State the blood parasite species.
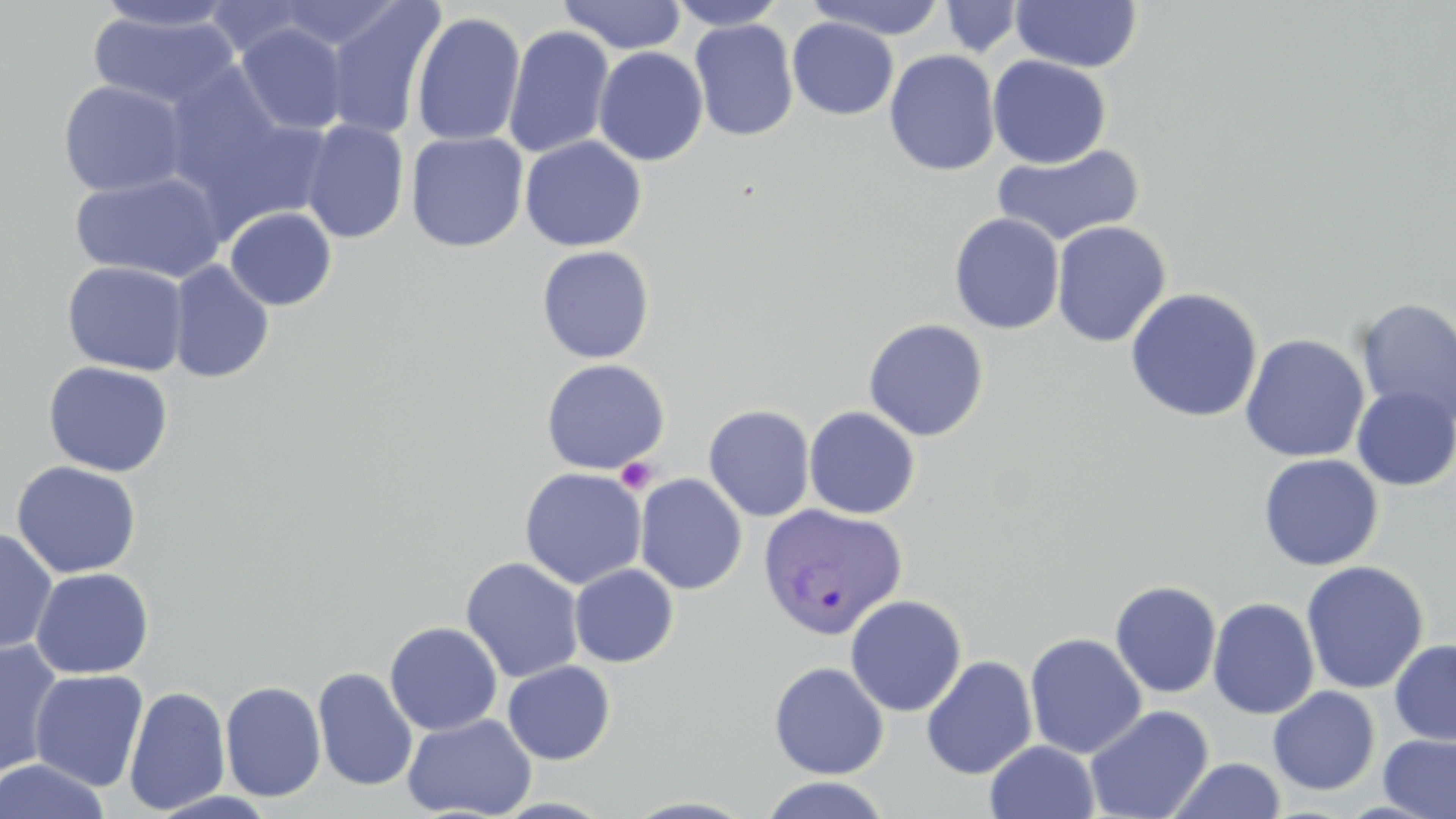
Plasmodium vivax.

Approximate bounding boxes as [x1, y1, x2, y2] in pixels. Plasmodium vivax-infected red blood cell locations: [758, 502, 907, 639]. Uninfected red blood cell locations: [89, 0, 241, 33], [321, 0, 444, 141], [558, 0, 687, 54], [666, 0, 788, 30], [804, 0, 950, 40], [202, 1, 324, 60], [939, 1, 1025, 58], [1009, 1, 1144, 72], [87, 8, 242, 112], [410, 11, 526, 147], [786, 17, 898, 120], [689, 19, 799, 142], [234, 23, 351, 136], [503, 24, 614, 158], [593, 46, 709, 166], [884, 49, 1001, 177], [987, 55, 1112, 169], [158, 65, 306, 215], [56, 79, 190, 197], [192, 109, 339, 238], [300, 120, 409, 243], [406, 131, 528, 253], [520, 136, 646, 251], [992, 143, 1146, 248], [69, 171, 227, 282], [224, 206, 337, 311], [949, 212, 1064, 335], [1051, 220, 1171, 348], [536, 245, 656, 364], [61, 260, 190, 376], [167, 260, 275, 384], [1125, 287, 1263, 423], [1354, 297, 1456, 429], [863, 318, 989, 441], [1240, 333, 1370, 463], [540, 358, 669, 475], [42, 360, 174, 478], [1352, 386, 1456, 491], [703, 404, 816, 522], [803, 406, 921, 519], [1257, 454, 1384, 572], [11, 460, 141, 579], [519, 467, 647, 590], [634, 473, 747, 595], [0, 528, 58, 654], [460, 557, 585, 683], [1300, 560, 1430, 695], [569, 564, 679, 667], [30, 567, 154, 679], [1109, 580, 1222, 699], [845, 594, 967, 716], [1207, 597, 1320, 719], [384, 621, 502, 736], [1025, 632, 1147, 758], [0, 638, 65, 780], [1389, 638, 1456, 745], [921, 655, 1038, 779], [502, 660, 616, 765], [769, 661, 889, 779], [312, 667, 418, 792], [29, 669, 149, 792], [219, 680, 326, 802], [123, 685, 231, 815], [1267, 686, 1381, 795], [1084, 705, 1214, 819], [402, 713, 537, 819], [1378, 733, 1456, 819], [985, 740, 1100, 819], [0, 758, 111, 819], [1168, 758, 1285, 818], [759, 776, 893, 818], [148, 790, 280, 819]. Platelet locations: [615, 457, 657, 494]. 1000x magnification. Thin blood smear. Image is 1456×819 pixels. May-Grünwald-Giemsa stain. Optical microscopy. Single field of view.